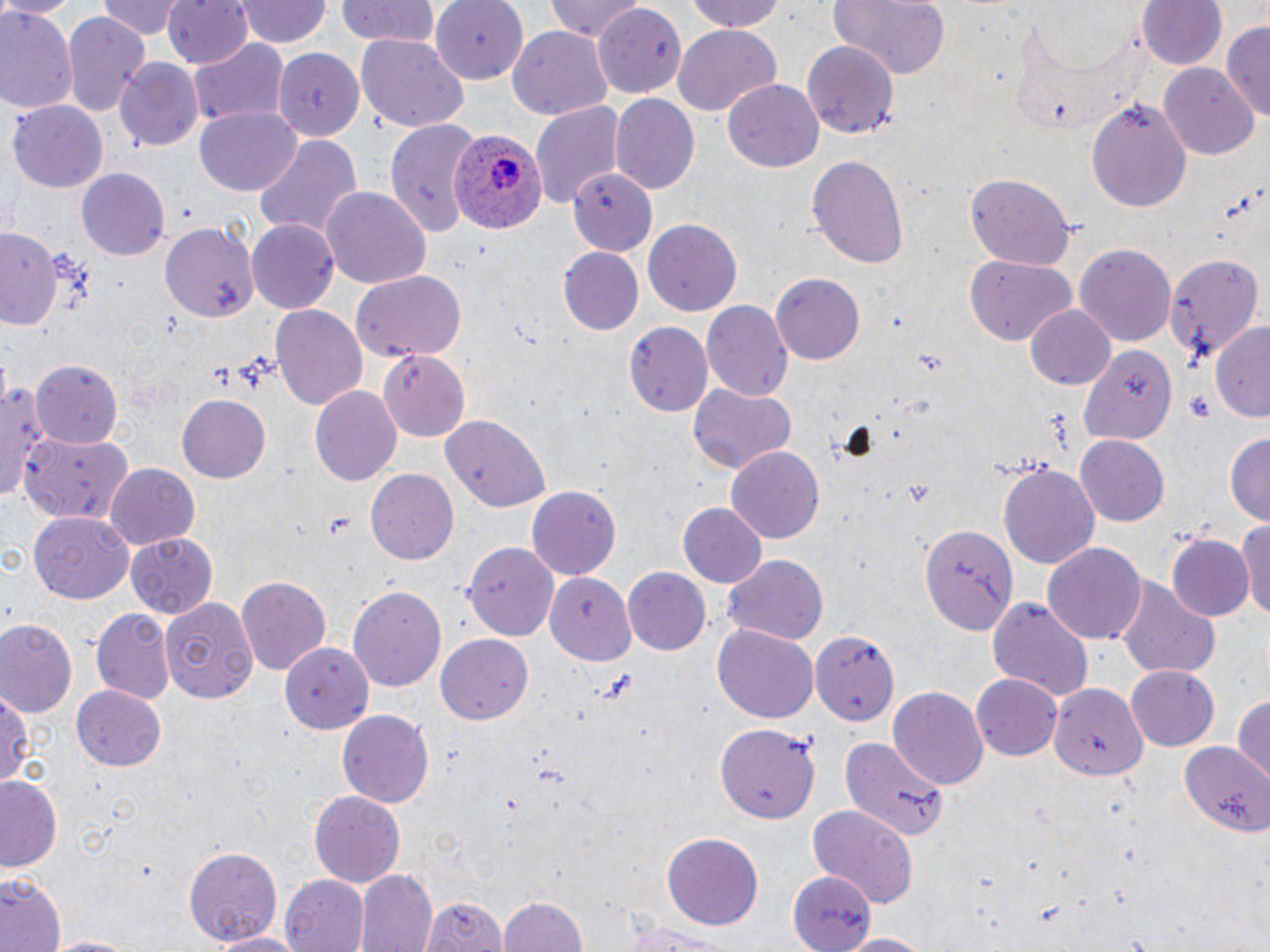
Summary:
  - Coordinate format: approximate bounding boxes as (x1, y1, x2, y2) in pixels
  - Uninfected red blood cell locations: (0, 0, 80, 18), (98, 0, 184, 39), (164, 0, 254, 69), (239, 0, 330, 48), (333, 0, 441, 49), (432, 0, 531, 83), (546, 0, 644, 43), (685, 0, 790, 34), (827, 0, 951, 77), (1138, 1, 1227, 72), (594, 6, 683, 99), (1, 8, 78, 115), (62, 12, 150, 116), (1223, 22, 1270, 120), (673, 26, 779, 115), (509, 27, 611, 120), (355, 34, 468, 134), (188, 37, 289, 130), (802, 40, 900, 141), (275, 50, 365, 141), (116, 59, 205, 152), (1160, 65, 1257, 158), (723, 79, 823, 173), (611, 95, 699, 193), (1086, 95, 1193, 213), (8, 100, 109, 193), (530, 101, 625, 209), (196, 105, 301, 194), (385, 119, 480, 236), (253, 136, 362, 242), (807, 155, 910, 269), (75, 167, 169, 261), (568, 170, 656, 254), (962, 172, 1076, 271), (321, 186, 432, 292), (158, 217, 261, 325), (247, 219, 341, 314), (644, 220, 742, 318), (0, 224, 63, 329), (1075, 241, 1178, 347), (557, 247, 643, 336), (1165, 252, 1264, 364), (964, 255, 1077, 344), (350, 269, 468, 363), (772, 272, 865, 364), (700, 301, 793, 402), (270, 302, 367, 412), (1024, 304, 1116, 392), (1209, 321, 1270, 421), (624, 322, 713, 418), (1079, 344, 1174, 442), (377, 351, 468, 439), (32, 361, 122, 445), (0, 379, 51, 500), (688, 383, 796, 477), (310, 388, 402, 488), (176, 393, 270, 484), (442, 418, 551, 514), (20, 430, 135, 524), (1224, 430, 1270, 527), (1076, 435, 1169, 526), (725, 446, 824, 543), (104, 463, 200, 549), (997, 463, 1099, 570), (366, 469, 462, 564), (527, 486, 620, 581), (677, 502, 768, 589), (1236, 512, 1270, 622), (30, 514, 133, 602), (921, 523, 1018, 635), (125, 532, 219, 618), (1170, 534, 1253, 621), (463, 540, 558, 642), (1042, 543, 1146, 645), (721, 555, 828, 647), (624, 567, 713, 656), (234, 575, 330, 678), (548, 577, 637, 662), (1116, 577, 1221, 682), (348, 586, 445, 691), (986, 596, 1095, 704), (162, 597, 260, 703), (90, 607, 175, 705), (2, 620, 78, 716), (712, 623, 819, 723), (812, 628, 899, 727), (434, 632, 533, 724), (273, 642, 372, 736), (1123, 664, 1220, 752), (971, 674, 1062, 760), (1049, 682, 1148, 779), (888, 685, 989, 789), (72, 686, 167, 771), (0, 688, 30, 789), (1232, 692, 1269, 787), (337, 709, 434, 809), (716, 721, 820, 822), (837, 736, 949, 844), (1178, 743, 1270, 839), (0, 776, 62, 872), (309, 790, 405, 888), (804, 804, 919, 907), (661, 833, 765, 927), (184, 845, 281, 948), (787, 869, 875, 951), (359, 870, 437, 952), (0, 871, 65, 952), (280, 875, 370, 952), (420, 894, 508, 951), (499, 894, 590, 952), (619, 920, 737, 951), (207, 930, 311, 951), (835, 933, 933, 952), (38, 934, 147, 952)
  - Plasmodium ovale-infected red blood cell locations: (448, 129, 549, 236)
  - Slide-level diagnosis: Plasmodium ovale
  - Modality: optical microscopy
  - Preparation: thin blood smear
  - Image size: 1270×952 pixels
  - Magnification: 1000x
  - Field of view: single
  - Stain: May-Grünwald-Giemsa